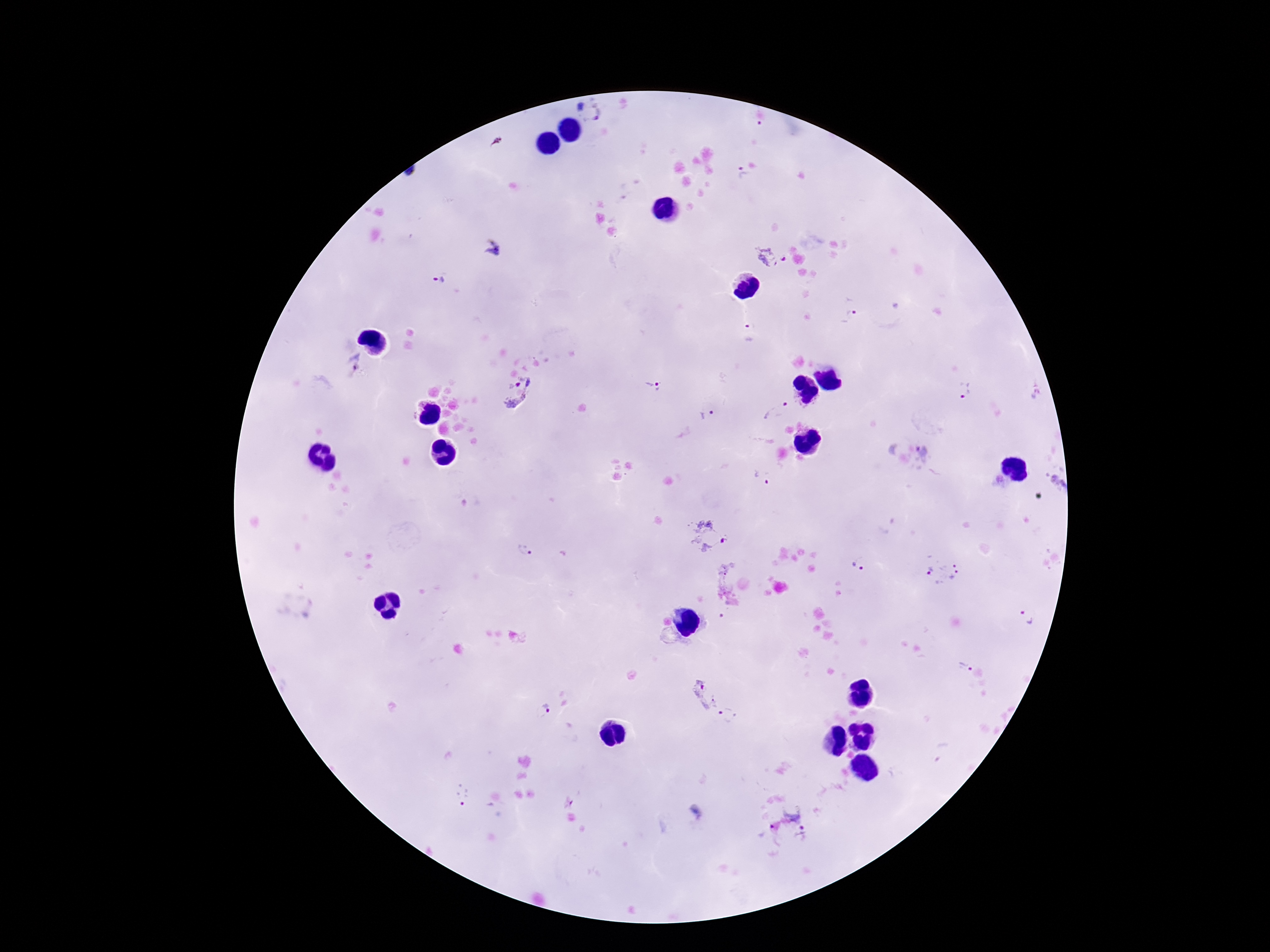 Approximate centers as {x, y} in pixels. Plasmodium parasite locations: {598, 112}, {742, 174}, {493, 247}, {773, 256}, {437, 280}, {851, 308}, {749, 332}, {352, 363}, {653, 387}, {968, 391}, {520, 392}, {775, 412}, {707, 415}, {926, 457}, {759, 476}, {705, 533}, {526, 550}, {861, 564}, {942, 574}, {1027, 617}, {963, 666}, {704, 695}, {546, 710}, {729, 716}, {462, 797}, {795, 820}. 100x magnification. One field from this slide. Photographed through the microscope eyepiece with a smartphone camera. Image is 1270×952 pixels. Thick blood smear. Giemsa-stained preparation. Patient malaria status: positive.